Report the malaria status of this cell.
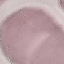

It is uninfected.

Summary:
  - Stain: Giemsa
  - Preparation: thin blood film
  - Image type: cell patch, automatically extracted from a larger field of view and resized to 64 × 64 pixels
  - Capture: smartphone through the microscope eyepiece